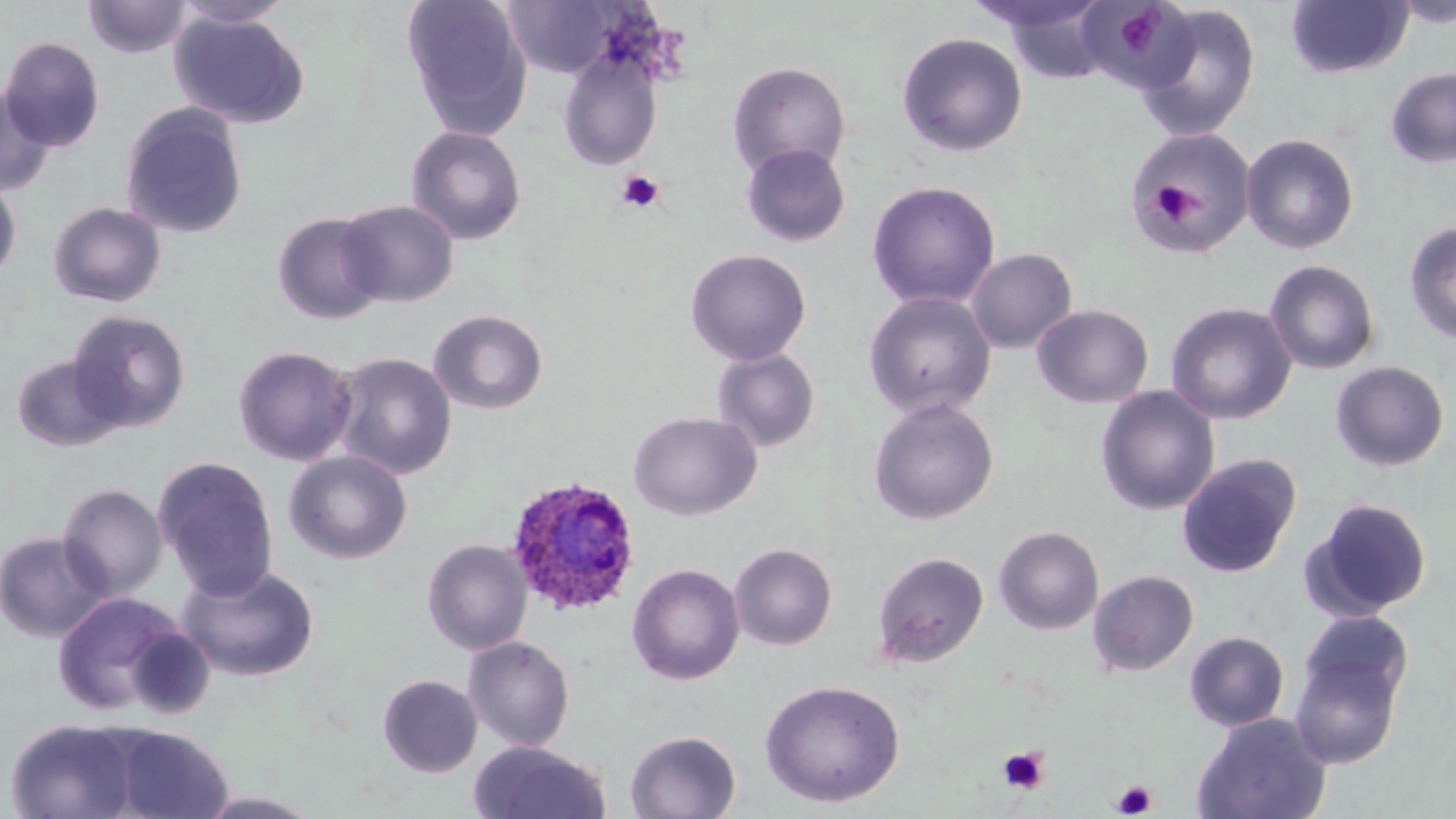

slide_level_diagnosis: Plasmodium ovale
magnification: 1000x
stain: May-Grünwald-Giemsa
uninfected_red_blood_cell_locations: 'approximate bounding boxes as (x1, y1, x2, y2) in pixels: (83, 0, 191, 59), (172, 0, 296, 28), (403, 0, 532, 139), (503, 0, 616, 77), (1081, 0, 1192, 87), (1392, 0, 1456, 28), (968, 1, 1110, 36), (991, 1, 1116, 82), (1286, 1, 1413, 78), (1136, 4, 1260, 141), (169, 11, 309, 128), (896, 31, 1028, 157), (0, 36, 106, 152), (557, 49, 663, 171), (727, 61, 851, 179), (1385, 67, 1456, 168), (0, 87, 55, 197), (120, 102, 249, 239), (406, 126, 527, 245), (1127, 128, 1258, 256), (1241, 133, 1359, 254), (741, 143, 851, 247), (0, 173, 22, 287), (866, 180, 1001, 310), (336, 199, 460, 307), (47, 201, 167, 307), (272, 212, 386, 325), (1404, 221, 1456, 344), (685, 248, 811, 366), (966, 248, 1077, 354), (1264, 259, 1380, 375), (863, 291, 997, 419), (1165, 302, 1297, 425), (1032, 304, 1154, 408), (428, 309, 548, 415), (67, 310, 191, 433), (233, 345, 358, 466), (712, 348, 821, 453), (332, 352, 457, 480), (11, 354, 127, 453), (1330, 360, 1450, 472), (1096, 386, 1220, 516), (868, 398, 999, 525), (629, 411, 763, 521), (283, 451, 413, 565), (1176, 452, 1303, 578), (153, 456, 280, 600), (57, 483, 167, 601), (1303, 498, 1433, 620), (993, 524, 1104, 634), (0, 530, 112, 643), (422, 538, 533, 655), (729, 543, 838, 650), (872, 551, 989, 668), (177, 562, 320, 682), (626, 563, 745, 685), (1087, 569, 1199, 676), (51, 591, 197, 719), (1297, 609, 1415, 711), (1184, 630, 1290, 731), (1288, 634, 1409, 768), (463, 636, 576, 752), (377, 674, 483, 777), (760, 678, 905, 807), (1192, 712, 1332, 819), (5, 718, 141, 818), (105, 725, 233, 819), (624, 729, 742, 818), (470, 741, 614, 819), (194, 790, 328, 818)'
modality: optical microscopy
plasmodium_ovale_infected_red_blood_cell_locations: 'approximate bounding boxes as (x1, y1, x2, y2) in pixels: (506, 476, 641, 616)'
platelet_locations: 'approximate bounding boxes as (x1, y1, x2, y2) in pixels: (1121, 13, 1168, 53), (616, 169, 665, 213), (1150, 181, 1197, 227), (997, 746, 1050, 794), (1112, 779, 1156, 817)'
image_size: 1456×819 pixels
field_of_view: single
preparation: thin blood film